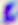
identification = Toxoplasma gondii
magnification = 400x
modality = photomicrograph